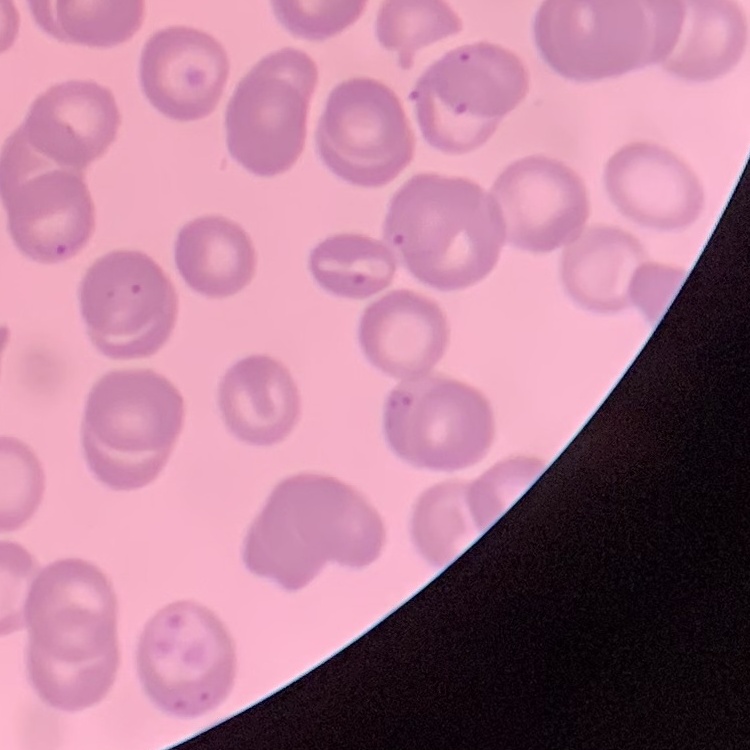

Summary:
  - Erythrocyte morphology: no rouleaux formation
  - Stain: Field's or Giemsa
  - Preparation: thin blood smear
  - Image type: square crop of a larger photomicrograph